Assess the morphology of the erythrocytes.
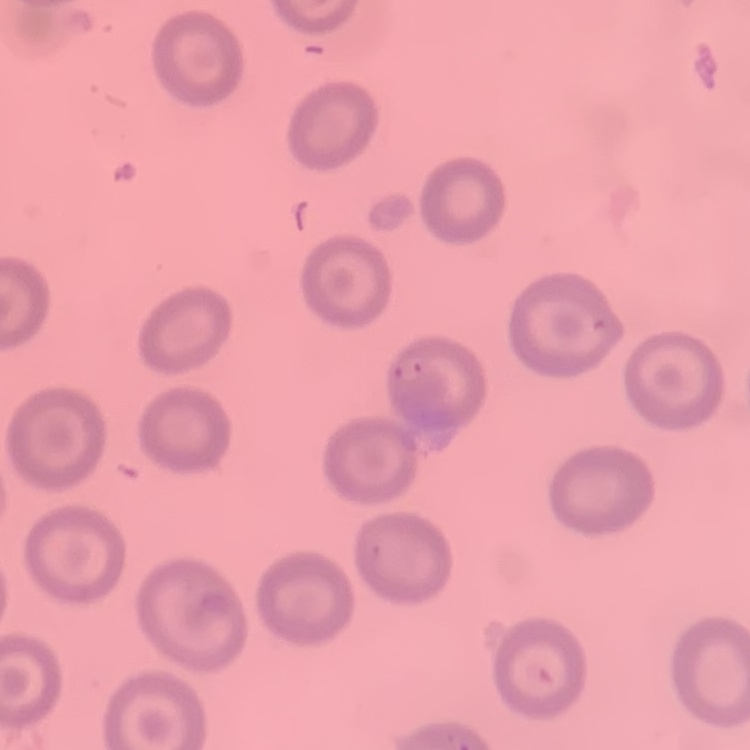

No rouleaux formation.

Summary:
  - Image type: square crop of a larger photomicrograph
  - Stain: Field's or Giemsa
  - Preparation: thin blood smear